Name the parasite shown.
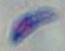

This is Toxoplasma gondii.

Captured at 1000x magnification. Micrograph.